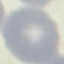
result = negative for malaria parasites
image type = automatically extracted cell patch, resized to 64 × 64 pixels
stain = Giemsa
preparation = thin blood film
capture = smartphone camera at the microscope eyepiece